Give the position of every Plasmodium parasite.
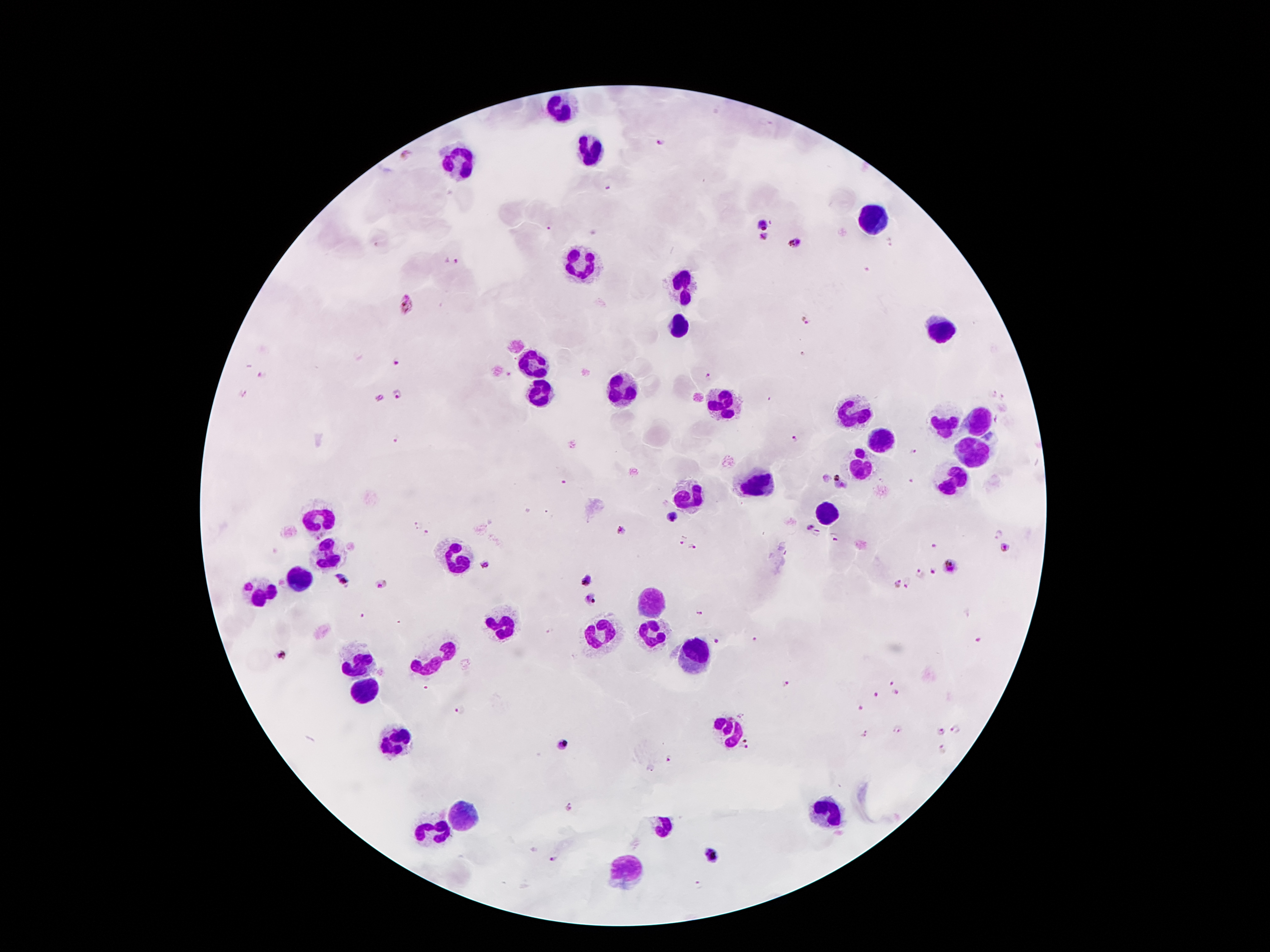
Approximate centers as {x, y} in pixels.
Plasmodium parasites: {659, 142}, {609, 188}, {764, 223}, {547, 226}, {764, 237}, {796, 242}, {891, 242}, {451, 259}, {408, 304}, {808, 321}, {802, 353}, {395, 361}, {263, 376}, {707, 378}, {244, 392}, {991, 393}, {399, 395}, {379, 398}, {1004, 399}, {997, 419}, {395, 439}, {792, 439}, {914, 451}, {842, 483}, {672, 517}, {417, 526}, {809, 527}, {621, 529}, {817, 533}, {428, 534}, {997, 534}, {835, 537}, {680, 540}, {933, 544}, {693, 546}, {1006, 547}, {484, 563}, {952, 565}, {933, 571}, {917, 575}, {341, 578}, {587, 581}, {909, 583}, {380, 584}, {898, 584}, {592, 599}, {717, 644}, {280, 654}, {788, 683}, {891, 683}, {895, 692}, {874, 695}, {861, 708}, {458, 710}, {957, 728}, {897, 730}, {940, 731}, {864, 732}, {563, 745}, {745, 746}, {942, 748}, {668, 759}, {711, 854}, {552, 858}.

leukocyte locations = {561, 107}, {589, 147}, {459, 160}, {872, 222}, {576, 259}, {680, 286}, {676, 321}, {941, 326}, {530, 363}, {534, 390}, {620, 390}, {726, 401}, {852, 407}, {978, 420}, {941, 423}, {879, 443}, {976, 451}, {861, 462}, {950, 478}, {755, 482}, {691, 498}, {824, 509}, {318, 515}, {324, 553}, {457, 557}, {298, 577}, {260, 588}, {653, 601}, {499, 622}, {603, 629}, {652, 634}, {694, 655}, {429, 661}, {361, 664}, {361, 689}, {734, 732}, {394, 741}, {463, 813}, {828, 813}, {429, 829}, {627, 869}
field of view = single
capture = smartphone camera through the microscope eyepiece
preparation = thick blood smear
patient malaria status = infected with Plasmodium falciparum
stain = Giemsa
magnification = 100x
image size = 1270×952 pixels